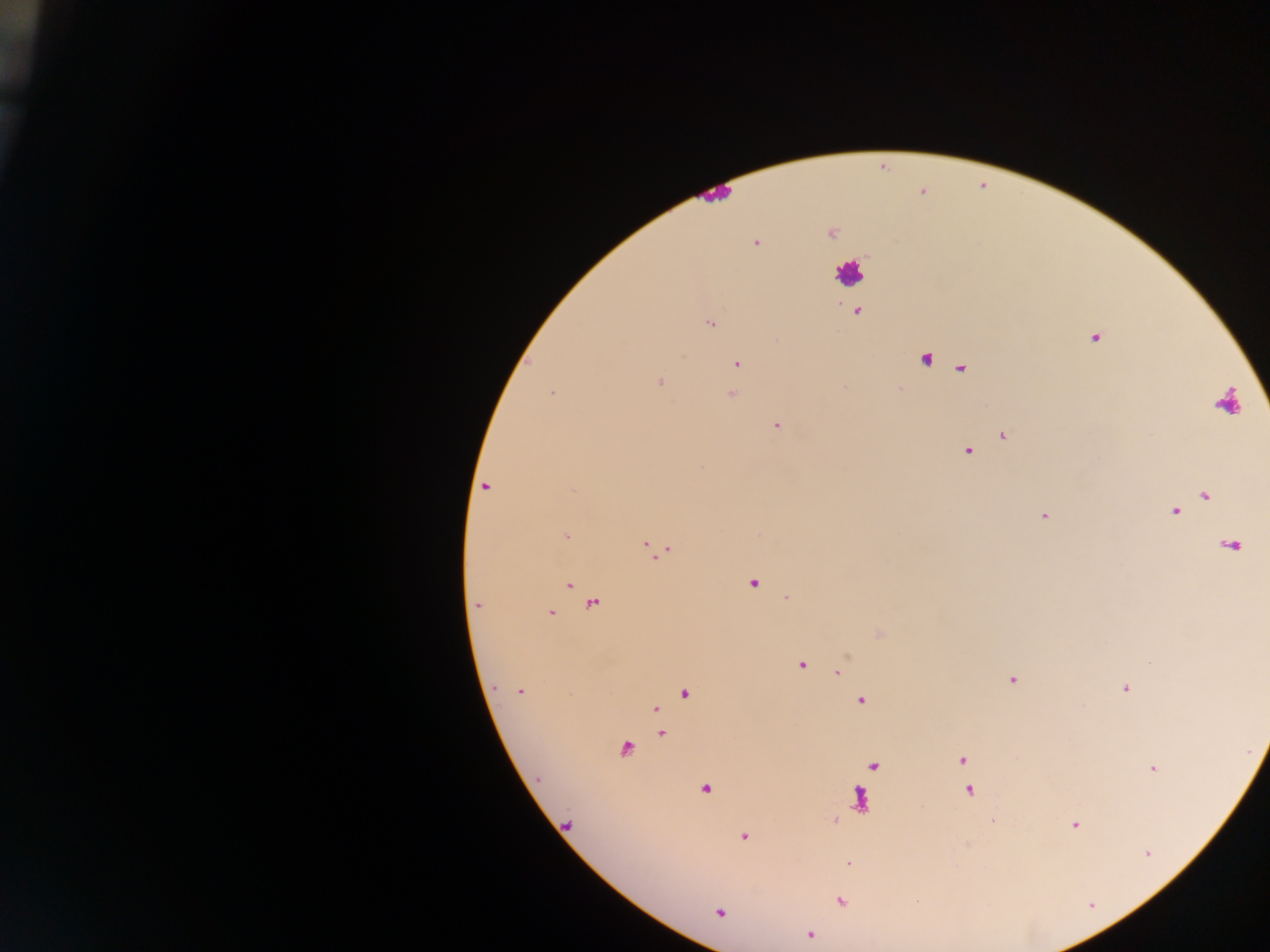

Approximate centers as [x, y] in pixels.
Summary:
  - Leukocyte locations: [850, 272], [1231, 402]
  - Plasmodium parasite locations: [831, 232], [756, 243], [856, 312], [710, 324], [1095, 338], [925, 358], [737, 364], [660, 382], [553, 393], [731, 395], [776, 426], [1003, 436], [967, 452], [486, 488], [1205, 495], [1176, 511], [1044, 515], [566, 536], [653, 548], [753, 584], [567, 585], [477, 605], [593, 605], [551, 613], [801, 665], [837, 672], [1012, 680], [1125, 690], [520, 691], [684, 694], [860, 702], [655, 710], [661, 734], [625, 749], [963, 760], [875, 764], [1154, 769], [706, 788], [968, 791], [859, 799], [1075, 825], [744, 836], [1148, 853], [848, 862], [840, 902], [720, 912], [810, 935]
  - Image size: 1270×952 pixels
  - Country: Ghana
  - Preparation: thick blood film
  - Field of view: single
  - Capture: mobile-phone photograph through a microscope